Report the malaria status of this cell.
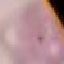
It is uninfected.

stain = Giemsa
capture = smartphone through the microscope eyepiece
image type = automatically extracted cell patch, resized to 64 × 64 pixels
preparation = thin smear